Locate platelets.
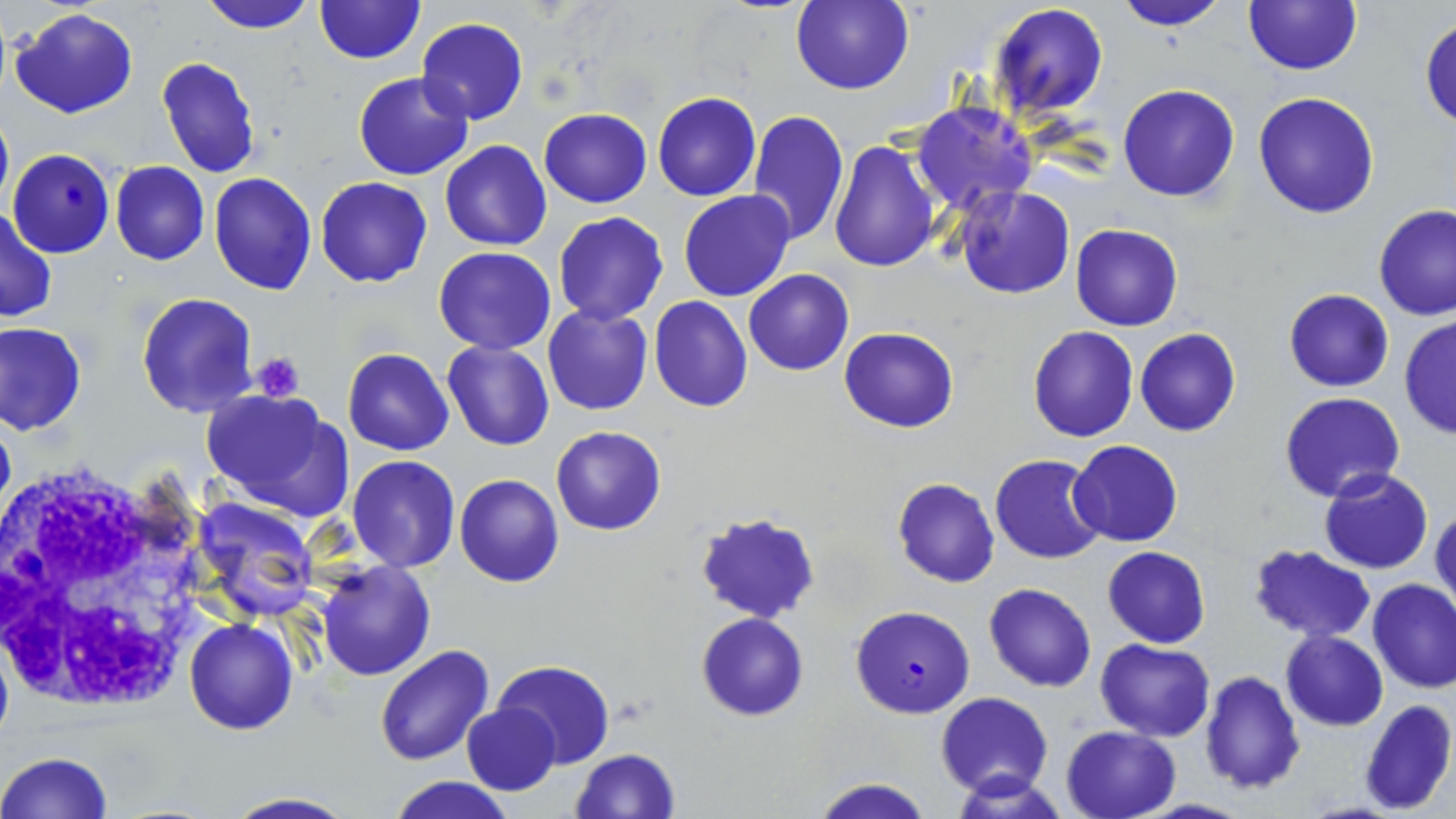

Approximate bounding boxes as (x1, y1, x2, y2) in pixels.
Platelets: (251, 353, 306, 401).

slide_level_diagnosis: Plasmodium falciparum
image_size: 1456×819 pixels
stain: May-Grünwald-Giemsa
plasmodium_falciparum_infected_red_blood_cell_locations: 'approximate bounding boxes as (x1, y1, x2, y2) in pixels: (851, 606, 974, 718)'
modality: light microscopy
uninfected_red_blood_cell_locations: 'approximate bounding boxes as (x1, y1, x2, y2) in pixels: (198, 0, 318, 34), (313, 0, 426, 65), (792, 0, 913, 94), (1111, 0, 1231, 31), (1243, 0, 1363, 75), (989, 3, 1109, 118), (10, 7, 139, 119), (1421, 17, 1455, 127), (416, 18, 528, 124), (156, 56, 260, 177), (353, 69, 474, 179), (1119, 84, 1239, 202), (1253, 91, 1380, 218), (653, 92, 760, 201), (911, 101, 1038, 214), (0, 108, 13, 218), (539, 108, 651, 208), (746, 108, 849, 247), (828, 139, 941, 270), (440, 140, 551, 251), (8, 149, 113, 257), (110, 161, 209, 266), (208, 173, 317, 294), (317, 177, 432, 287), (955, 186, 1075, 299), (679, 190, 795, 302), (0, 204, 56, 324), (1374, 205, 1456, 320), (554, 213, 669, 325), (1070, 224, 1182, 331), (433, 247, 556, 354), (743, 269, 853, 376), (1285, 289, 1394, 392), (136, 292, 261, 418), (650, 296, 752, 412), (542, 305, 652, 416), (1399, 317, 1456, 439), (0, 322, 87, 435), (840, 325, 958, 433), (1028, 325, 1138, 441), (1134, 328, 1241, 437), (441, 341, 556, 451), (343, 349, 454, 456), (198, 389, 354, 520), (1280, 393, 1405, 504), (551, 425, 666, 535), (1068, 440, 1182, 547), (989, 453, 1107, 564), (347, 455, 461, 573), (1319, 469, 1434, 575), (456, 474, 562, 587), (893, 478, 998, 587), (190, 497, 321, 623), (1432, 502, 1455, 612), (695, 510, 819, 621), (1248, 543, 1375, 644), (1103, 546, 1211, 648), (315, 561, 435, 681), (1366, 579, 1456, 694), (983, 582, 1097, 692), (698, 612, 808, 721), (184, 617, 298, 735), (1280, 630, 1387, 731), (0, 636, 13, 753), (1097, 639, 1215, 740), (374, 644, 494, 766), (493, 660, 616, 769), (1198, 670, 1305, 794), (936, 691, 1052, 800), (1359, 699, 1455, 815), (461, 705, 561, 795), (1061, 724, 1181, 819), (570, 748, 680, 818), (0, 752, 114, 819), (389, 776, 515, 819), (810, 777, 934, 819), (222, 793, 356, 819)'
preparation: thin blood film
white_blood_cell_locations: 'approximate bounding boxes as (x1, y1, x2, y2) in pixels: (0, 455, 221, 714)'
magnification: 1000x
field_of_view: single